Comment on the morphology of the erythrocytes.
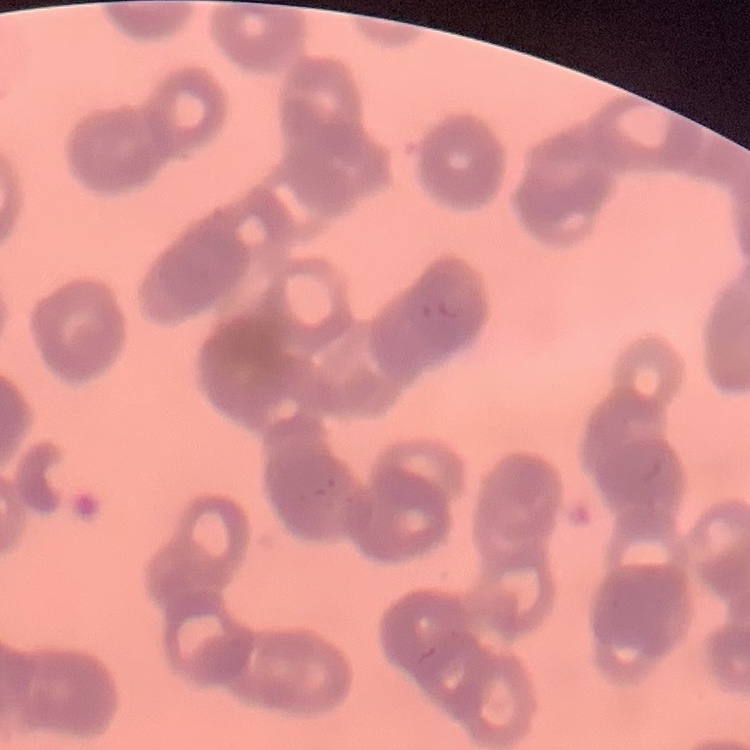
They show rouleaux formation.

Square crop of a larger photomicrograph. Field's or Giemsa stain. Thin blood smear.